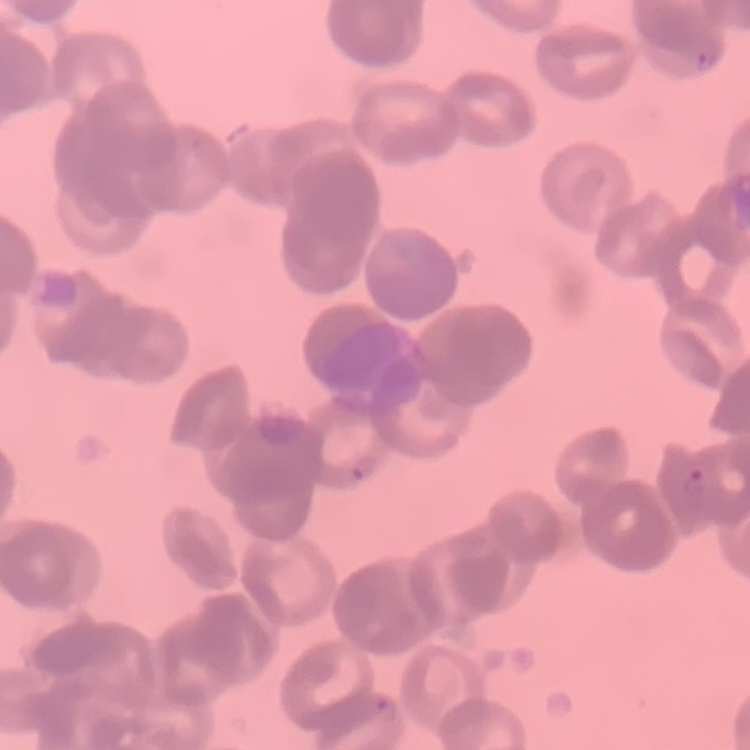
erythrocyte_morphology: rouleaux formation
stain: Field's or Giemsa
image_type: one tile cut from a larger photomicrograph
preparation: thin peripheral smear